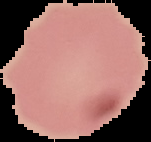

image type = segmented cell region on a black background
preparation = thin blood smear
result = negative for malaria parasites
image size = 151×142 pixels